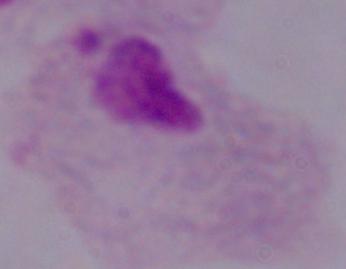
Summary:
  - Magnification: 1000x
  - Identification: trichomonad
  - Modality: micrograph